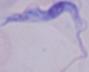 Photomicrograph. A trypanosome is seen. Captured at 1000x magnification.